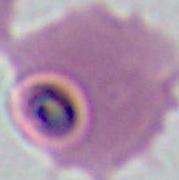

identification = Plasmodium
magnification = 400x or 1000x
modality = micrograph